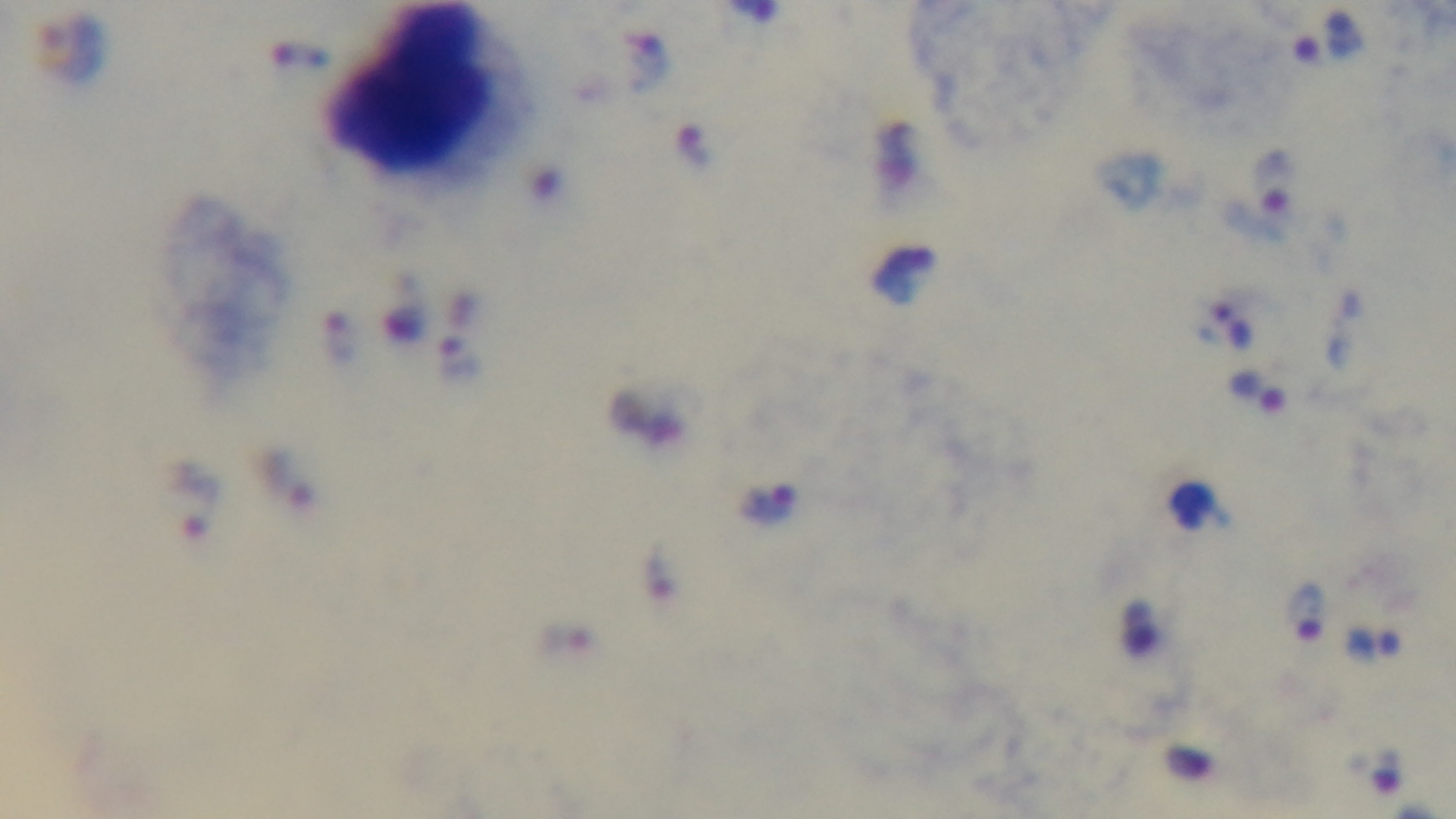 Mounted 4K digital camera. Malaria status: positive. Photomicrograph. Preparation: thick smear. 100x oil-immersion objective. Giemsa stain. Single field of view.